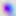 Photomicrograph. Toxoplasma gondii is seen. 400x magnification.